Locate every Plasmodium parasite.
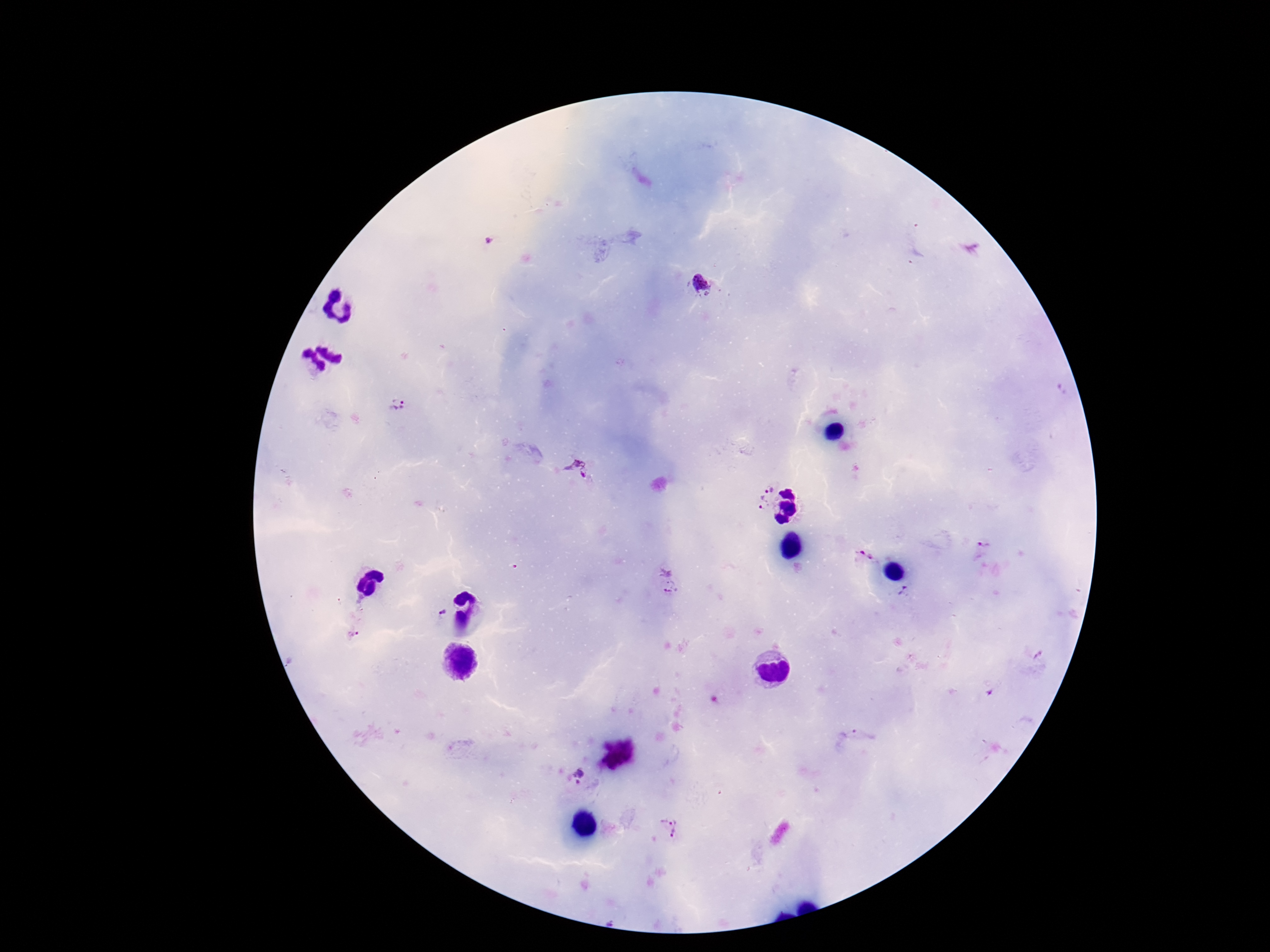
Approximate centers as [x, y] in pixels.
Plasmodium parasites: [489, 242], [702, 284], [401, 405], [579, 470], [758, 489], [981, 547], [859, 553], [668, 582], [907, 594], [441, 614], [352, 633], [855, 736], [574, 776], [669, 829].

Summary:
  - Image size: 1270×952 pixels
  - Patient malaria status: infected
  - Stain: Giemsa
  - Preparation: thick peripheral-blood smear
  - Capture: smartphone camera through the microscope eyepiece
  - Magnification: 100x
  - Field of view: one from this slide